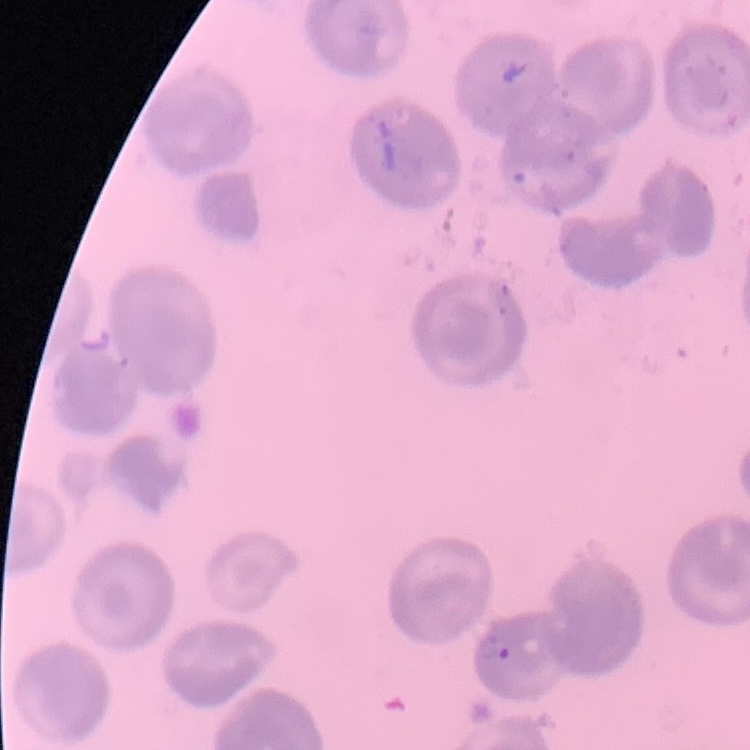
red blood cell morphology = no rouleaux formation
stain = Field's or Giemsa
preparation = thin peripheral smear
image type = one tile cut from a larger photomicrograph